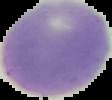

image_size: 112×100 pixels
image_type: segmented cell region on a black background
malaria_status: uninfected
preparation: thin blood film